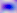
Captured at 400x magnification. Photomicrograph. Toxoplasma gondii is seen.